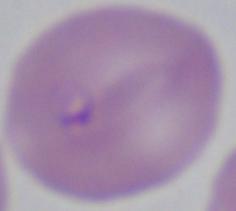

magnification = 1000x
modality = micrograph
identification = Babesia